Point out each Plasmodium parasite.
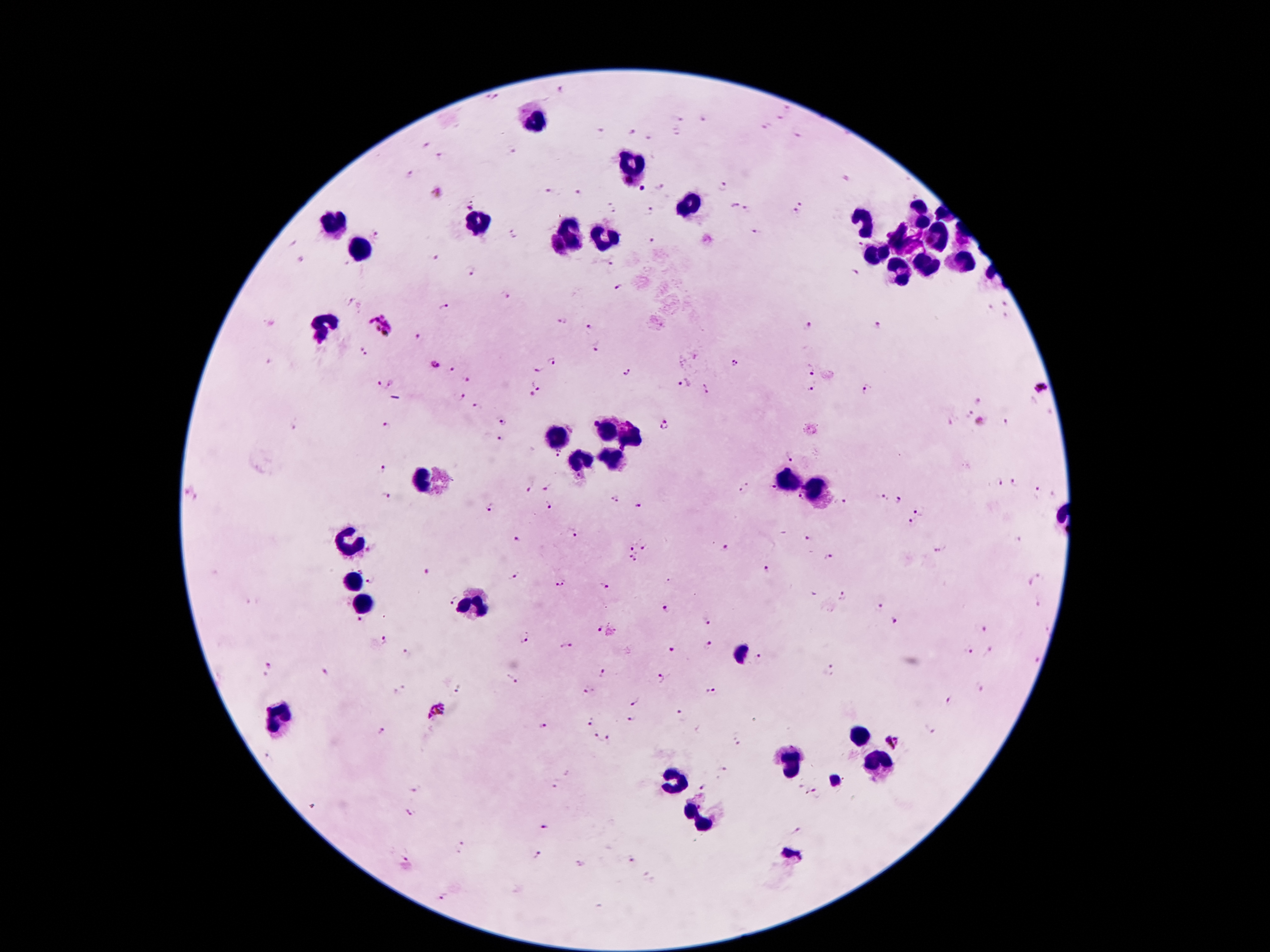
Approximate centers as [x, y] in pixels.
Plasmodium parasites: [562, 92], [485, 98], [497, 98], [787, 109], [780, 119], [680, 120], [704, 120], [768, 124], [601, 131], [632, 132], [674, 132], [798, 135], [649, 139], [426, 144], [515, 150], [441, 157], [412, 173], [847, 179], [659, 187], [723, 187], [642, 189], [436, 193], [549, 193], [577, 193], [801, 203], [731, 205], [611, 206], [469, 209], [748, 210], [651, 211], [796, 211], [753, 231], [514, 232], [376, 236], [294, 242], [650, 243], [859, 244], [550, 249], [435, 258], [301, 259], [610, 265], [469, 271], [857, 272], [618, 289], [504, 297], [351, 302], [1006, 303], [447, 308], [991, 308], [1007, 315], [562, 322], [379, 325], [809, 325], [877, 325], [590, 328], [418, 336], [596, 349], [362, 353], [551, 361], [735, 362], [434, 364], [453, 369], [810, 369], [538, 370], [626, 371], [467, 378], [682, 383], [379, 384], [390, 384], [538, 385], [1041, 388], [705, 389], [813, 389], [868, 390], [460, 396], [531, 396], [978, 400], [476, 408], [967, 412], [1009, 419], [503, 421], [979, 422], [290, 425], [667, 425], [385, 426], [499, 439], [792, 456], [381, 470], [997, 482], [1015, 483], [528, 487], [549, 487], [744, 489], [772, 489], [1038, 492], [193, 494], [384, 496], [799, 497], [880, 497], [612, 501], [898, 501], [841, 503], [547, 506], [640, 506], [491, 508], [919, 510], [911, 522], [572, 532], [807, 538], [515, 539], [630, 548], [643, 548], [724, 548], [937, 549], [371, 551], [828, 556], [628, 558], [634, 561], [764, 568], [428, 571], [513, 577], [372, 578], [1034, 578], [559, 582], [602, 588], [844, 596], [451, 600], [1039, 604], [881, 607], [668, 608], [708, 620], [357, 622], [894, 622], [599, 628], [1046, 630], [986, 632], [522, 639], [383, 640], [566, 646], [707, 646], [672, 651], [966, 651], [990, 652], [404, 654], [760, 660], [1035, 660], [271, 666], [829, 672], [326, 674], [604, 674], [663, 677], [511, 679], [980, 688], [459, 689], [401, 692], [588, 692], [714, 693], [951, 701], [631, 702], [679, 709], [438, 710], [632, 720], [589, 722], [544, 726], [931, 730], [383, 733], [598, 739], [736, 739], [612, 740], [893, 741], [721, 772], [555, 785], [704, 785], [416, 787], [816, 793], [412, 813], [546, 825], [798, 830], [459, 846], [406, 853], [536, 854], [631, 861], [446, 897].

Leukocyte locations: [528, 121], [631, 170], [694, 203], [913, 216], [481, 222], [334, 224], [862, 224], [568, 238], [934, 240], [605, 242], [901, 242], [360, 245], [874, 256], [962, 261], [922, 265], [895, 273], [327, 321], [605, 431], [633, 436], [554, 437], [610, 461], [579, 463], [421, 478], [787, 483], [813, 490], [346, 546], [353, 582], [364, 601], [477, 605], [280, 714], [859, 735], [793, 761], [875, 765], [677, 777], [702, 817]. Thick blood smear. Giemsa stain. Patient malaria status: infected with Plasmodium falciparum. 100x magnification. Image is 1270×952 pixels. Single field of view. Photographed through the microscope eyepiece with a smartphone camera.